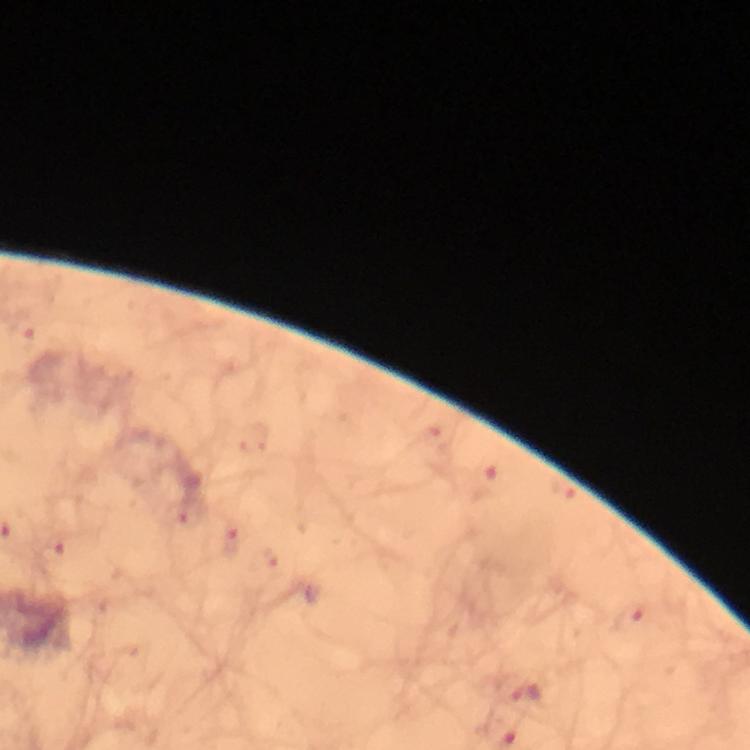

context: from a diagnostic examination for malaria
cropped_from: one field of view
immersion_oil: applied
stain: Giemsa
capture: smartphone camera through the microscope
image_size: 750×750 pixels
magnification: 100x
preparation: thick smear
malaria_parasite_locations: 'approximate centers as {x, y} in pixels: {23, 333}, {53, 554}, {525, 691}'